Point out each Plasmodium parasite.
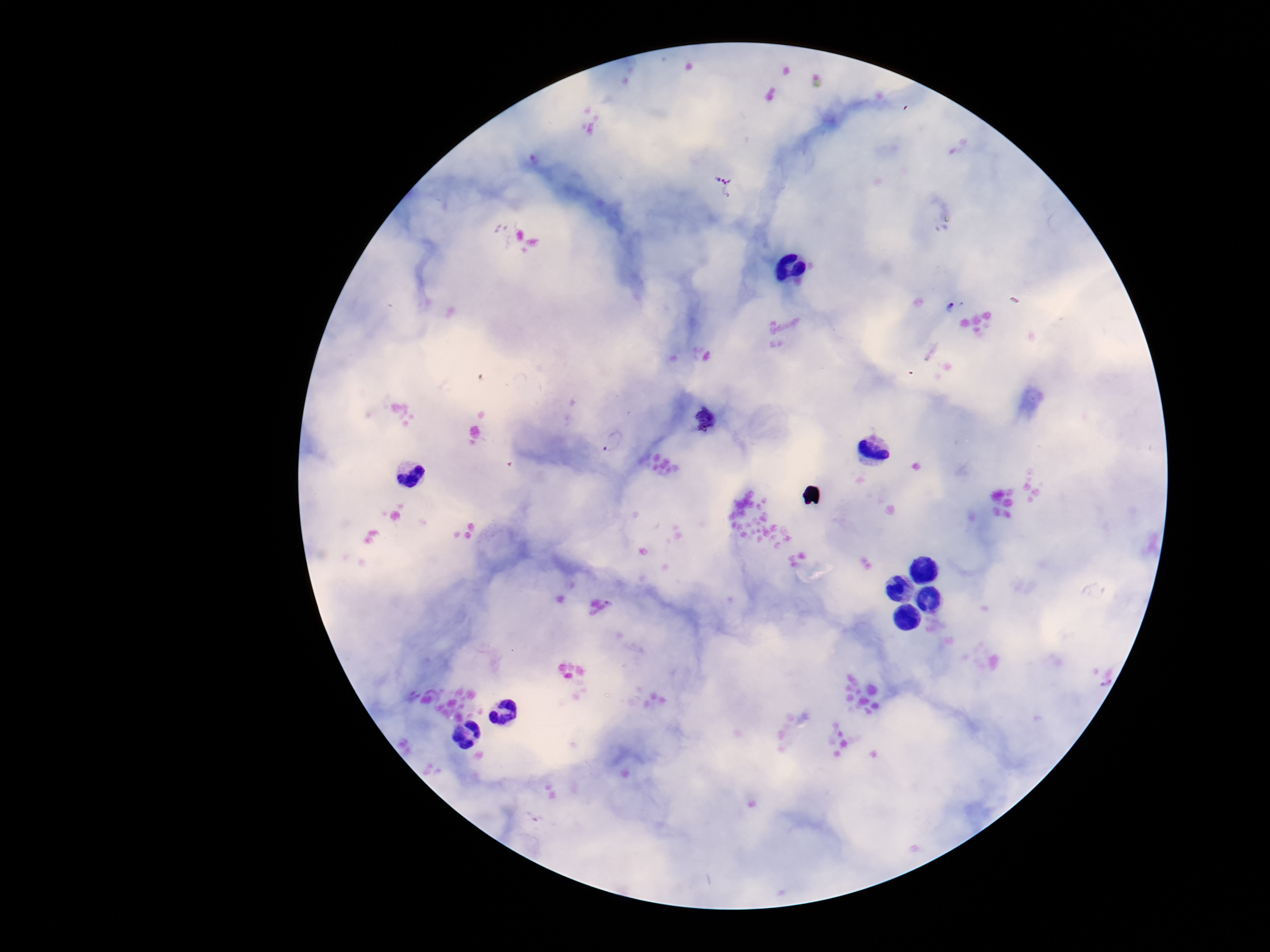

Approximate object centers, in pixels from the top-left corner.
Plasmodium parasites: (x=724, y=184), (x=950, y=308), (x=613, y=441).

{
  "patient_malaria_status": "infected",
  "magnification": "100x",
  "stain": "Giemsa",
  "capture": "smartphone camera through the microscope eyepiece",
  "image_size": "1270×952 pixels",
  "preparation": "thick peripheral-blood smear",
  "field_of_view": "single"
}